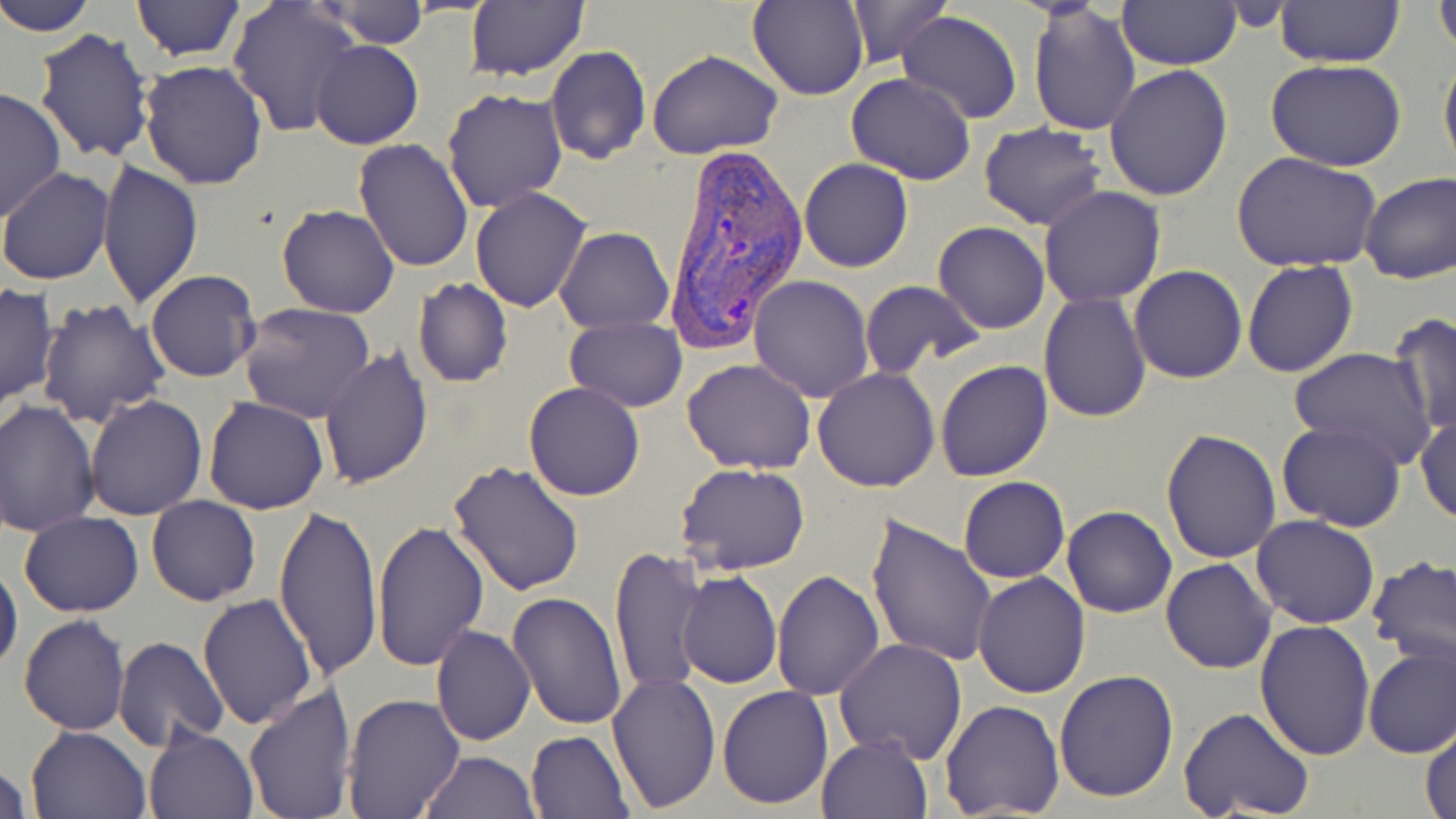

{
  "slide_level_diagnosis": "Plasmodium vivax",
  "modality": "light microscopy",
  "plasmodium_vivax_infected_red_blood_cell_locations": "approximate bounding boxes as [x1, y1, x2, y2] in pixels: [662, 141, 808, 346]",
  "field_of_view": "single",
  "stain": "May-Grünwald-Giemsa",
  "uninfected_red_blood_cell_locations": "approximate bounding boxes as [x1, y1, x2, y2] in pixels: [2, 0, 98, 36], [128, 0, 249, 61], [843, 0, 950, 68], [1275, 0, 1406, 68], [1434, 0, 1456, 58], [314, 1, 429, 48], [748, 1, 870, 102], [1116, 1, 1238, 69], [227, 2, 363, 139], [464, 2, 590, 83], [1028, 3, 1142, 136], [895, 11, 1024, 124], [33, 28, 155, 164], [312, 41, 422, 149], [545, 46, 651, 163], [646, 49, 784, 161], [1439, 49, 1456, 179], [139, 59, 270, 190], [1265, 59, 1408, 169], [1105, 63, 1233, 203], [846, 74, 977, 185], [0, 85, 66, 223], [440, 87, 567, 212], [979, 122, 1107, 230], [353, 138, 475, 272], [1233, 153, 1382, 274], [799, 158, 913, 272], [96, 161, 204, 309], [0, 167, 114, 286], [1358, 172, 1456, 285], [1038, 186, 1165, 308], [470, 187, 593, 313], [276, 203, 399, 317], [932, 221, 1051, 334], [555, 226, 674, 332], [1242, 260, 1359, 379], [1129, 265, 1248, 383], [146, 270, 261, 383], [748, 275, 875, 401], [411, 279, 513, 388], [858, 280, 984, 378], [0, 283, 57, 412], [1040, 292, 1152, 423], [35, 299, 172, 429], [240, 303, 376, 423], [1387, 312, 1455, 438], [564, 317, 687, 411], [318, 347, 434, 487], [1288, 347, 1437, 467], [683, 358, 817, 474], [934, 360, 1053, 482], [813, 367, 940, 492], [524, 382, 645, 501], [83, 393, 207, 520], [203, 396, 328, 514], [1, 400, 101, 537], [1415, 413, 1456, 525], [1276, 420, 1405, 532], [1161, 427, 1284, 563], [447, 458, 587, 596], [676, 463, 809, 575], [958, 476, 1070, 584], [146, 495, 262, 606], [274, 498, 382, 687], [1061, 505, 1177, 618], [19, 511, 143, 617], [1251, 514, 1379, 629], [865, 515, 999, 669], [373, 521, 490, 672], [609, 547, 708, 697], [1366, 555, 1456, 678], [1161, 558, 1276, 674], [0, 560, 23, 676], [677, 570, 782, 688], [771, 570, 884, 701], [972, 571, 1090, 698], [198, 591, 317, 730], [507, 592, 627, 730], [19, 614, 131, 735], [1255, 620, 1376, 760], [430, 626, 535, 746], [114, 637, 230, 751], [833, 637, 967, 765], [1363, 644, 1456, 759], [1054, 669, 1179, 803], [606, 674, 721, 813], [243, 685, 355, 818], [717, 685, 833, 811], [340, 693, 465, 818], [939, 700, 1066, 819], [1178, 706, 1314, 819], [1421, 721, 1456, 819], [25, 726, 151, 818], [144, 726, 258, 819], [526, 731, 633, 818], [816, 733, 932, 819], [418, 751, 541, 818], [0, 759, 33, 817]",
  "preparation": "thin blood smear",
  "image_size": "1456×819 pixels",
  "magnification": "1000x"
}